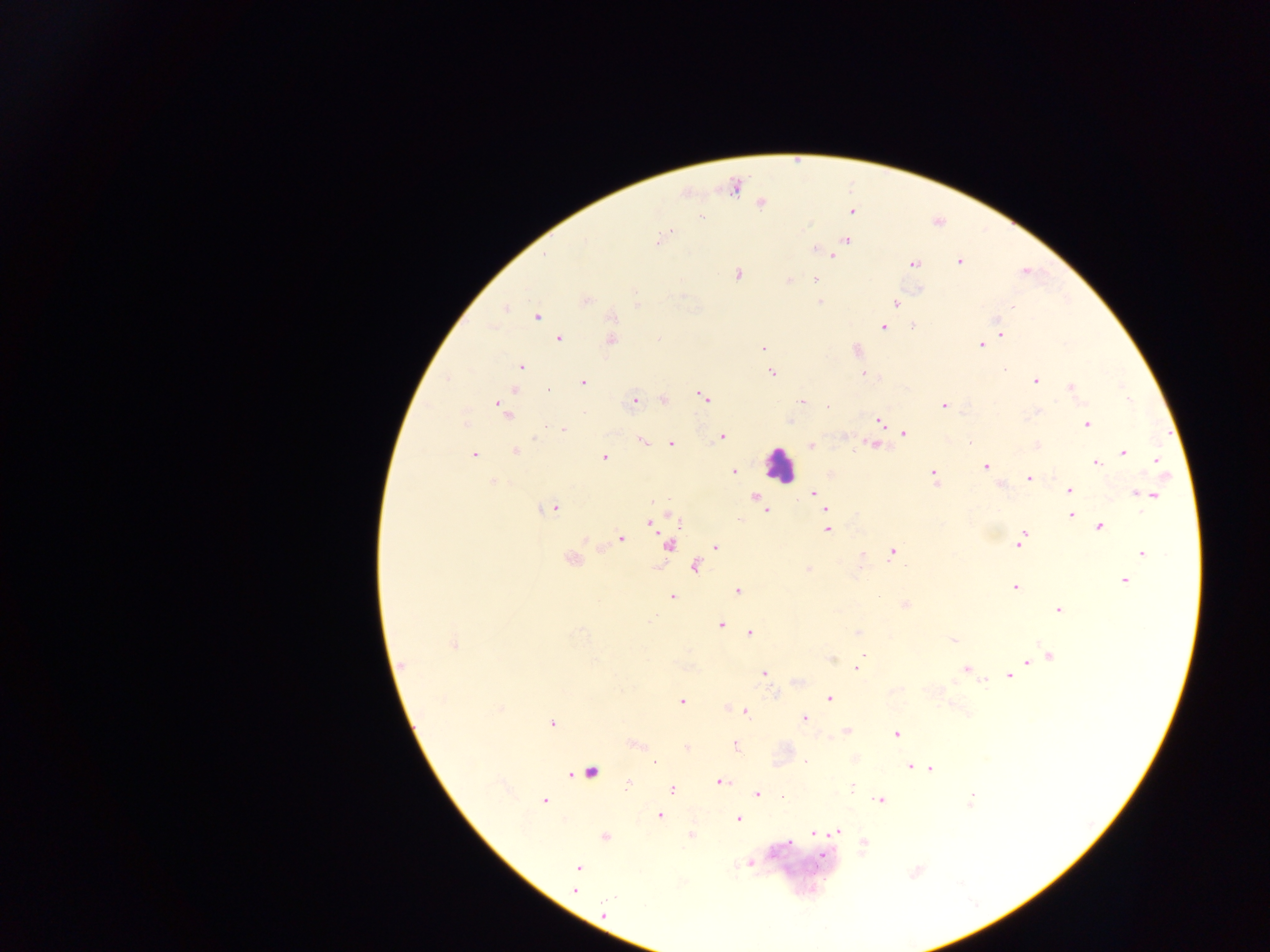
Approximate centers as (x, y) in pixels. Leukocyte locations: (779, 466). Plasmodium parasite locations: (734, 187), (760, 203), (851, 211), (700, 216), (670, 231), (658, 240), (847, 240), (584, 241), (835, 251), (545, 255), (832, 256), (959, 262), (914, 263), (737, 275), (815, 279), (789, 280), (586, 300), (819, 302), (895, 303), (636, 305), (1013, 306), (506, 308), (537, 316), (612, 317), (883, 327), (1001, 334), (559, 339), (610, 340), (980, 345), (762, 348), (521, 367), (1003, 371), (771, 373), (863, 374), (1035, 380), (583, 382), (1071, 388), (513, 390), (547, 390), (703, 397), (1128, 399), (664, 400), (635, 401), (801, 402), (828, 406), (943, 406), (503, 410), (788, 421), (878, 421), (465, 424), (1086, 424), (563, 429), (904, 434), (721, 437), (642, 441), (970, 442), (671, 444), (875, 445), (811, 446), (1036, 446), (515, 451), (1124, 453), (474, 455), (605, 458), (1156, 461), (1096, 463), (986, 467), (733, 472), (933, 475), (1028, 477), (493, 482), (1000, 484), (1069, 490), (813, 493), (1138, 493), (1151, 495), (754, 497), (657, 500), (762, 507), (553, 508), (766, 510), (826, 510), (1071, 515), (650, 523), (1100, 527), (827, 530), (621, 539), (1022, 539), (669, 545), (716, 547), (892, 552), (1141, 553), (571, 559), (694, 567), (808, 569), (1124, 581), (1014, 587), (737, 590), (672, 597), (905, 605), (1059, 609), (720, 624), (749, 633), (857, 633), (953, 640), (453, 644), (862, 655), (1049, 656), (1040, 657), (1027, 662), (403, 665), (858, 665), (966, 669), (763, 673), (1009, 675), (829, 698), (442, 700), (682, 702), (745, 712), (804, 718), (552, 723), (846, 731), (896, 735), (634, 745), (735, 746), (686, 747), (806, 762), (655, 763), (910, 767), (931, 769), (591, 772), (721, 782), (627, 786), (672, 788), (851, 788), (756, 794), (970, 799), (879, 800), (543, 801), (660, 815), (738, 818), (838, 832), (814, 834), (605, 837), (822, 855), (750, 863), (577, 867), (574, 889), (603, 914). Image is 1270×952 pixels. Thick blood film. Photographed through a microscope with a mobile-phone camera. Collected in Ghana. One field of view.